Name the blood parasite species.
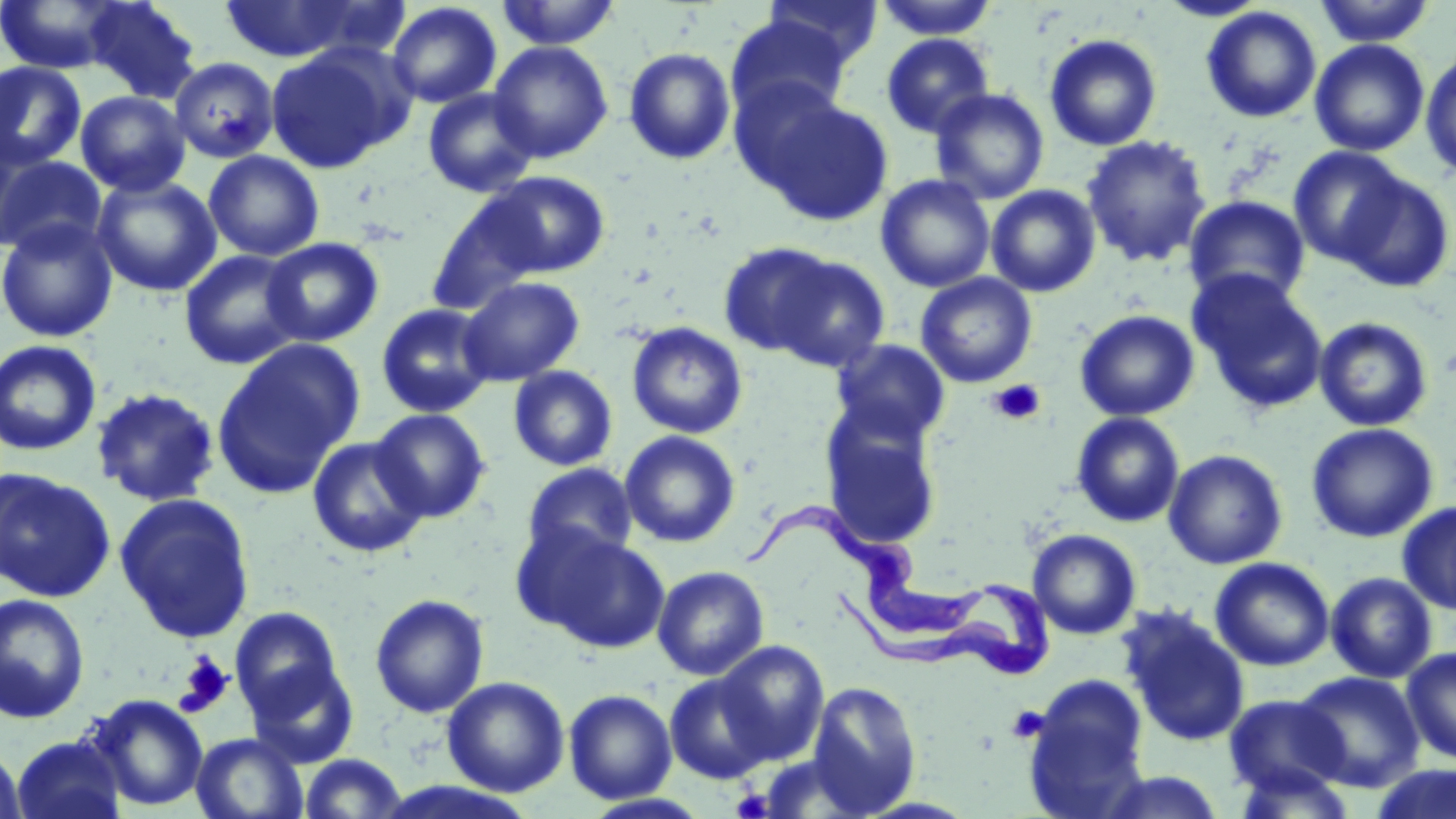

Trypanosoma brucei.

Summary:
  - Coordinate format: approximate bounding boxes as (x1, y1, x2, y2) in pixels
  - Uninfected red blood cell locations: (81, 0, 201, 102), (218, 0, 382, 64), (496, 0, 621, 50), (763, 0, 882, 71), (1156, 0, 1269, 22), (0, 1, 125, 74), (874, 1, 1000, 40), (1312, 1, 1437, 47), (386, 2, 502, 109), (1201, 6, 1321, 123), (726, 15, 852, 122), (881, 33, 995, 139), (1044, 33, 1162, 151), (1309, 39, 1430, 157), (488, 41, 613, 163), (264, 43, 412, 173), (622, 47, 736, 165), (1420, 51, 1456, 180), (169, 57, 280, 163), (0, 61, 86, 172), (422, 88, 539, 199), (929, 88, 1050, 204), (75, 91, 191, 197), (758, 95, 893, 225), (1082, 134, 1212, 267), (1288, 146, 1411, 266), (203, 150, 324, 261), (1, 154, 106, 258), (1334, 168, 1455, 293), (480, 171, 610, 278), (91, 174, 221, 297), (875, 174, 995, 292), (986, 184, 1101, 297), (425, 193, 550, 315), (1183, 195, 1311, 306), (0, 217, 119, 343), (262, 236, 384, 347), (716, 242, 840, 358), (179, 249, 306, 370), (768, 255, 890, 372), (1189, 271, 1328, 412), (915, 273, 1037, 387), (458, 276, 584, 386), (375, 302, 497, 418), (1074, 309, 1200, 421), (1314, 316, 1434, 432), (626, 322, 748, 438), (0, 339, 102, 455), (212, 339, 363, 498), (830, 339, 951, 447), (507, 365, 618, 471), (91, 387, 221, 507), (370, 408, 491, 522), (1071, 412, 1184, 527), (821, 413, 942, 549), (1306, 422, 1438, 543), (620, 431, 741, 548), (307, 436, 429, 559), (1163, 449, 1288, 569), (522, 463, 637, 564), (0, 468, 115, 602), (115, 493, 255, 643), (1398, 501, 1456, 616), (527, 527, 670, 654), (1028, 529, 1141, 639), (1210, 557, 1334, 671), (652, 565, 770, 680), (1326, 571, 1438, 683), (0, 593, 90, 723), (369, 593, 489, 718), (229, 607, 346, 724), (1120, 609, 1250, 747), (716, 642, 829, 764), (1401, 647, 1456, 764), (244, 659, 359, 768), (1295, 671, 1425, 792), (665, 672, 775, 784), (442, 676, 570, 797), (1024, 677, 1150, 814), (804, 680, 922, 815), (563, 688, 677, 804), (1223, 693, 1348, 797), (87, 695, 208, 812), (191, 733, 308, 818), (11, 735, 126, 819), (0, 742, 28, 819), (298, 753, 410, 818), (1229, 762, 1359, 818), (1368, 764, 1456, 819), (1096, 770, 1226, 818)
  - Trypanosoma brucei locations: (746, 496, 1056, 676)
  - Platelet locations: (988, 379, 1046, 424), (174, 653, 234, 717), (1006, 705, 1049, 743), (730, 787, 774, 818)
  - Magnification: 1000x
  - Modality: optical microscopy
  - Image size: 1456×819 pixels
  - Preparation: thin blood film
  - Field of view: single
  - Stain: May-Grünwald-Giemsa